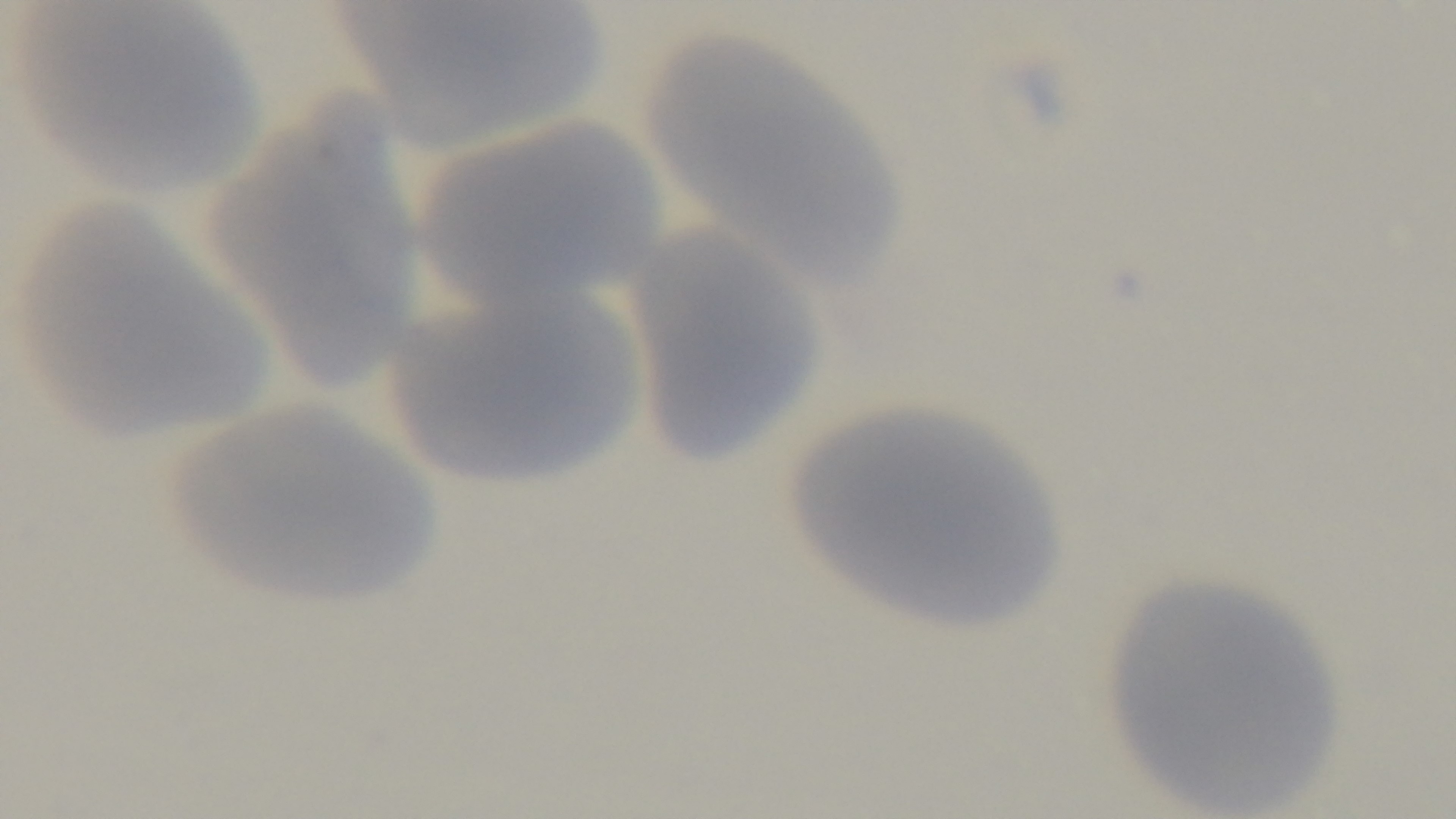

Malaria status: negative. One field from the slide. Preparation: thin. Light microscopy. Giemsa stain. Captured with a mounted 4K digital camera. Oil-immersion objective, 100x.